Locate every Plasmodium vivax-infected red blood cell.
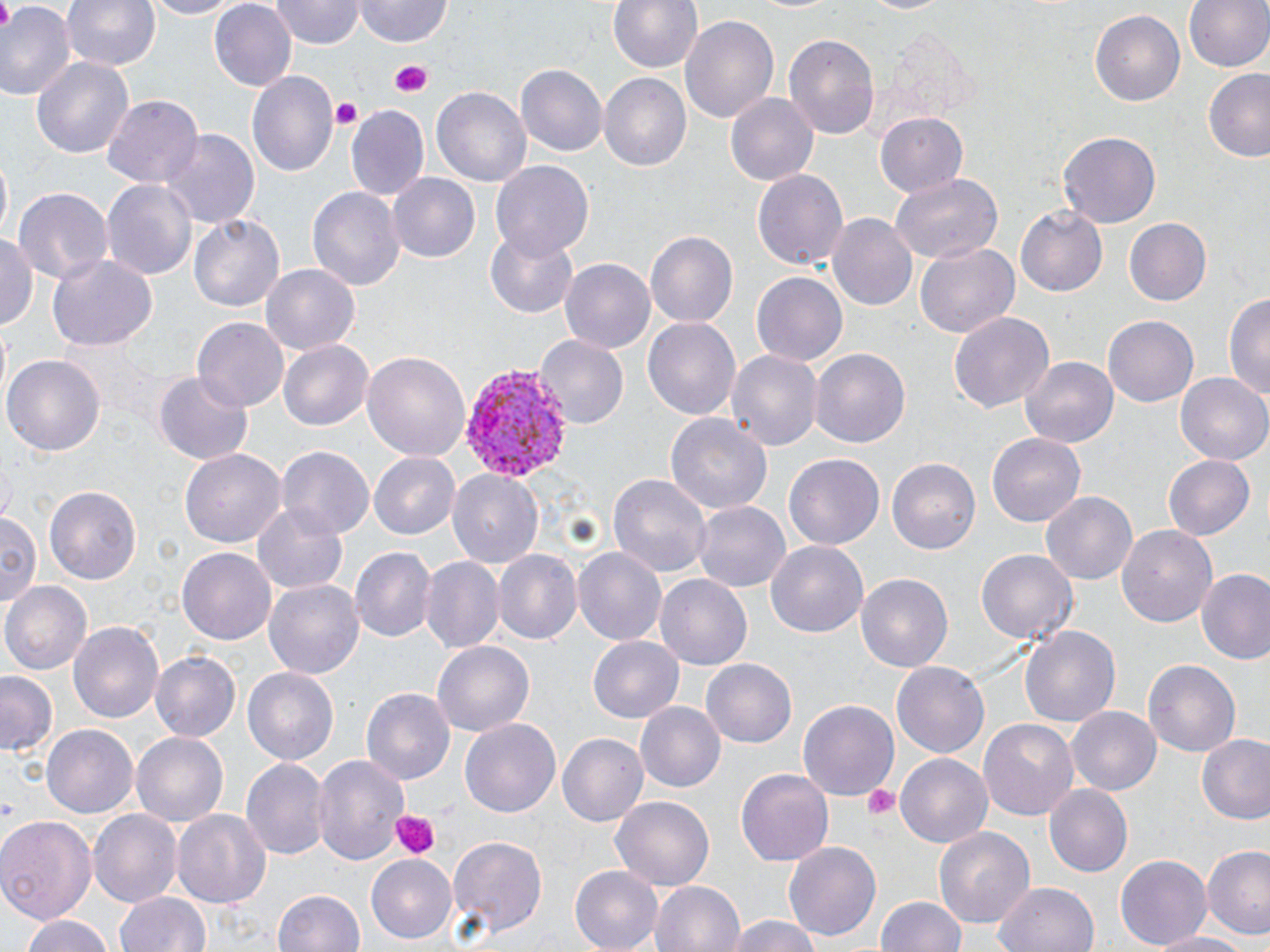
Approximate bounding boxes as named x1/y1/x2/y2 corners in pixels.
Plasmodium vivax-infected red blood cells: (x1=459, y1=363, x2=571, y2=485).

slide-level diagnosis = Plasmodium vivax
preparation = thin blood film
magnification = 1000x
stain = May-Grünwald-Giemsa
platelet locations = approximate bounding boxes as named x1/y1/x2/y2 corners in pixels: (x1=386, y1=59, x2=432, y2=97), (x1=330, y1=99, x2=364, y2=130), (x1=861, y1=782, x2=901, y2=821), (x1=391, y1=809, x2=440, y2=859)
uninfected red blood cell locations = approximate bounding boxes as named x1/y1/x2/y2 corners in pixels: (x1=63, y1=0, x2=160, y2=71), (x1=135, y1=0, x2=241, y2=18), (x1=357, y1=0, x2=451, y2=45), (x1=608, y1=0, x2=703, y2=76), (x1=858, y1=0, x2=957, y2=15), (x1=1184, y1=0, x2=1270, y2=76), (x1=270, y1=1, x2=363, y2=49), (x1=209, y1=3, x2=296, y2=91), (x1=0, y1=4, x2=73, y2=103), (x1=1088, y1=8, x2=1185, y2=106), (x1=680, y1=14, x2=781, y2=125), (x1=784, y1=32, x2=880, y2=139), (x1=884, y1=33, x2=978, y2=127), (x1=33, y1=56, x2=132, y2=158), (x1=516, y1=64, x2=608, y2=158), (x1=247, y1=71, x2=339, y2=180), (x1=1202, y1=71, x2=1270, y2=162), (x1=598, y1=73, x2=689, y2=173), (x1=433, y1=87, x2=531, y2=190), (x1=724, y1=93, x2=817, y2=188), (x1=102, y1=96, x2=202, y2=188), (x1=346, y1=106, x2=430, y2=201), (x1=873, y1=112, x2=971, y2=199), (x1=161, y1=127, x2=260, y2=232), (x1=1058, y1=129, x2=1163, y2=227), (x1=1, y1=159, x2=13, y2=240), (x1=490, y1=162, x2=594, y2=261), (x1=753, y1=169, x2=848, y2=272), (x1=388, y1=173, x2=481, y2=264), (x1=887, y1=173, x2=1002, y2=267), (x1=101, y1=176, x2=199, y2=284), (x1=307, y1=183, x2=405, y2=290), (x1=13, y1=186, x2=112, y2=285), (x1=1016, y1=206, x2=1107, y2=296), (x1=828, y1=212, x2=918, y2=310), (x1=190, y1=214, x2=284, y2=313), (x1=1122, y1=218, x2=1212, y2=307), (x1=486, y1=229, x2=578, y2=318), (x1=644, y1=230, x2=737, y2=329), (x1=0, y1=231, x2=38, y2=333), (x1=916, y1=243, x2=1019, y2=338), (x1=47, y1=252, x2=156, y2=349), (x1=560, y1=258, x2=655, y2=354), (x1=261, y1=263, x2=359, y2=356), (x1=751, y1=271, x2=847, y2=367), (x1=1226, y1=290, x2=1270, y2=407), (x1=948, y1=310, x2=1055, y2=414), (x1=1103, y1=315, x2=1198, y2=408), (x1=642, y1=316, x2=741, y2=422), (x1=193, y1=319, x2=287, y2=410), (x1=536, y1=335, x2=628, y2=429), (x1=278, y1=339, x2=373, y2=432), (x1=724, y1=347, x2=822, y2=452), (x1=809, y1=348, x2=911, y2=449), (x1=362, y1=351, x2=471, y2=463), (x1=5, y1=354, x2=104, y2=455), (x1=1020, y1=356, x2=1119, y2=447), (x1=156, y1=371, x2=254, y2=465), (x1=1177, y1=372, x2=1270, y2=466), (x1=665, y1=412, x2=772, y2=516), (x1=987, y1=433, x2=1086, y2=526), (x1=276, y1=446, x2=374, y2=540), (x1=180, y1=450, x2=286, y2=549), (x1=369, y1=451, x2=460, y2=541), (x1=785, y1=453, x2=884, y2=549), (x1=1164, y1=453, x2=1256, y2=541), (x1=1, y1=455, x2=16, y2=524), (x1=887, y1=457, x2=981, y2=554), (x1=449, y1=469, x2=544, y2=570), (x1=608, y1=470, x2=711, y2=576), (x1=42, y1=484, x2=141, y2=585), (x1=1040, y1=490, x2=1136, y2=586), (x1=253, y1=501, x2=350, y2=597), (x1=693, y1=502, x2=790, y2=595), (x1=0, y1=510, x2=42, y2=610), (x1=1117, y1=522, x2=1220, y2=627), (x1=766, y1=537, x2=868, y2=636), (x1=575, y1=546, x2=668, y2=646), (x1=178, y1=547, x2=275, y2=646), (x1=349, y1=547, x2=435, y2=644), (x1=492, y1=549, x2=582, y2=647), (x1=977, y1=549, x2=1077, y2=646), (x1=420, y1=556, x2=504, y2=653), (x1=1197, y1=569, x2=1270, y2=665), (x1=857, y1=572, x2=955, y2=673), (x1=655, y1=575, x2=752, y2=672), (x1=264, y1=579, x2=364, y2=682), (x1=2, y1=580, x2=90, y2=676), (x1=69, y1=618, x2=164, y2=724), (x1=1019, y1=624, x2=1121, y2=732), (x1=586, y1=636, x2=684, y2=724), (x1=432, y1=641, x2=534, y2=737), (x1=151, y1=650, x2=241, y2=742), (x1=1144, y1=659, x2=1239, y2=758), (x1=702, y1=660, x2=797, y2=747), (x1=892, y1=663, x2=989, y2=757), (x1=242, y1=666, x2=339, y2=766), (x1=0, y1=671, x2=58, y2=757), (x1=360, y1=688, x2=455, y2=787), (x1=798, y1=700, x2=900, y2=802), (x1=636, y1=704, x2=723, y2=790), (x1=1068, y1=706, x2=1161, y2=795), (x1=979, y1=716, x2=1080, y2=820), (x1=460, y1=717, x2=561, y2=819), (x1=42, y1=725, x2=138, y2=821), (x1=131, y1=730, x2=228, y2=826), (x1=558, y1=734, x2=648, y2=826), (x1=1197, y1=735, x2=1270, y2=825), (x1=312, y1=752, x2=409, y2=866), (x1=895, y1=753, x2=993, y2=850), (x1=243, y1=757, x2=327, y2=860), (x1=735, y1=767, x2=833, y2=867), (x1=1044, y1=784, x2=1133, y2=878), (x1=609, y1=793, x2=714, y2=892), (x1=174, y1=807, x2=273, y2=909), (x1=89, y1=810, x2=182, y2=908), (x1=0, y1=813, x2=96, y2=926), (x1=932, y1=825, x2=1035, y2=929), (x1=446, y1=835, x2=548, y2=940), (x1=784, y1=840, x2=882, y2=942), (x1=1203, y1=847, x2=1269, y2=939), (x1=364, y1=853, x2=457, y2=944), (x1=1114, y1=854, x2=1214, y2=950), (x1=570, y1=866, x2=666, y2=952), (x1=650, y1=880, x2=746, y2=952), (x1=993, y1=880, x2=1100, y2=952), (x1=273, y1=887, x2=370, y2=952), (x1=116, y1=893, x2=211, y2=952), (x1=875, y1=895, x2=968, y2=952), (x1=18, y1=914, x2=118, y2=952), (x1=724, y1=914, x2=824, y2=952), (x1=1148, y1=932, x2=1253, y2=952)
image size = 1270×952 pixels
modality = light microscopy
field of view = single